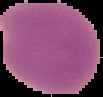
Cell region segmented out of the field of view; the surrounding area is masked to black. From a thin blood smear. Malaria status: parasitized. Image is 103×97 pixels.